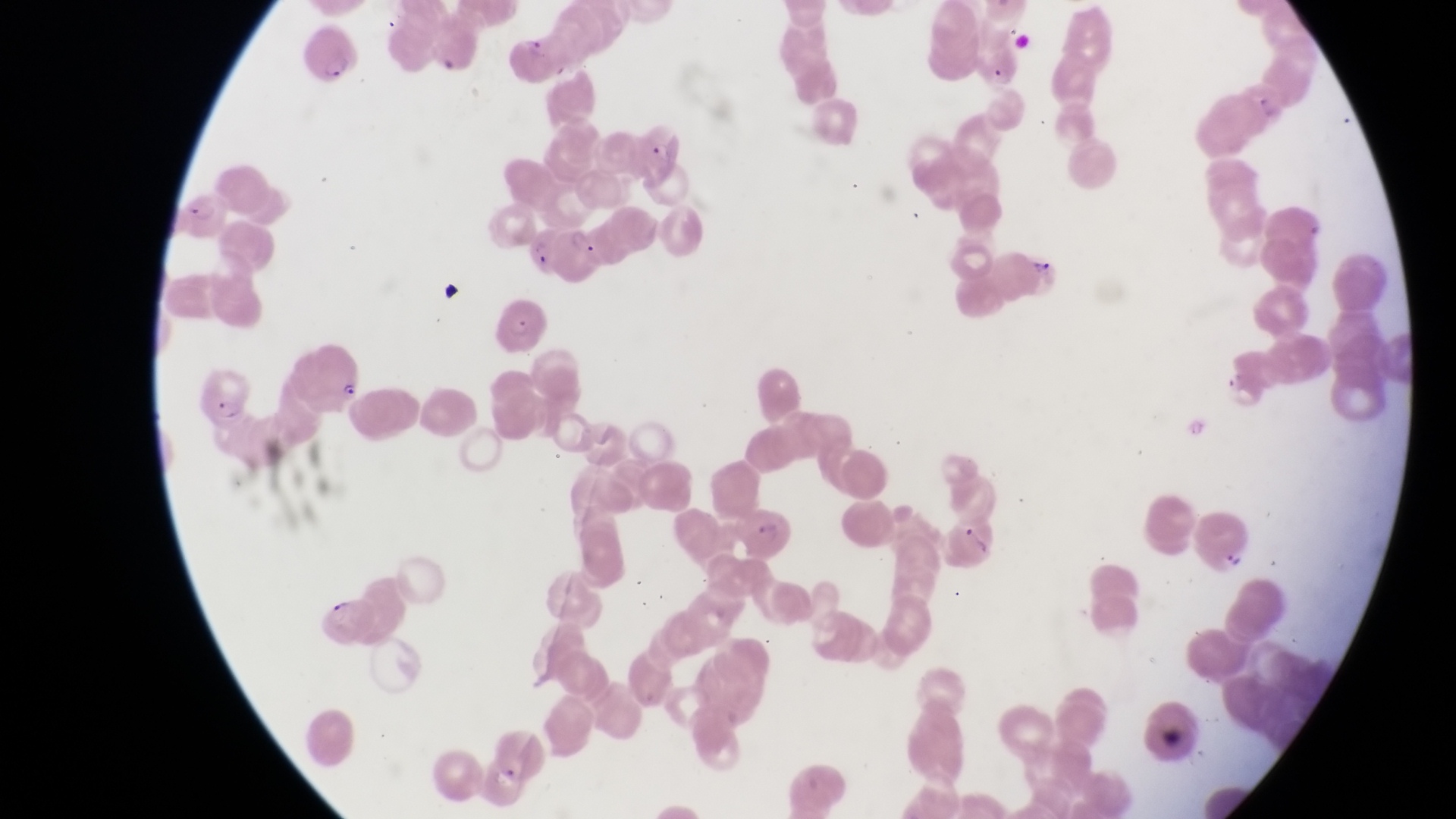

Approximate bounding boxes as {left, top, right, bottom} in pixels. Artifact (platelet-like body, stain precipitate, or debris) locations: {436, 274, 462, 306}, {959, 515, 993, 564}, {1159, 720, 1196, 756}. Parasitised red blood cell locations: {304, 32, 367, 92}, {508, 32, 560, 82}, {635, 115, 694, 187}, {179, 192, 232, 241}, {555, 227, 608, 286}, {1007, 241, 1065, 297}, {489, 294, 549, 352}, {287, 337, 367, 416}, {192, 362, 256, 421}, {724, 505, 800, 558}, {1185, 510, 1254, 569}. Sample from Uganda. Single field of view. At a magnification of 1000x. Thin blood smear. Image is 1456×819 pixels. Photographed through the eyepiece of an Olympus CX-23 microscope with a smartphone camera.